Assess the morphology of the erythrocytes.
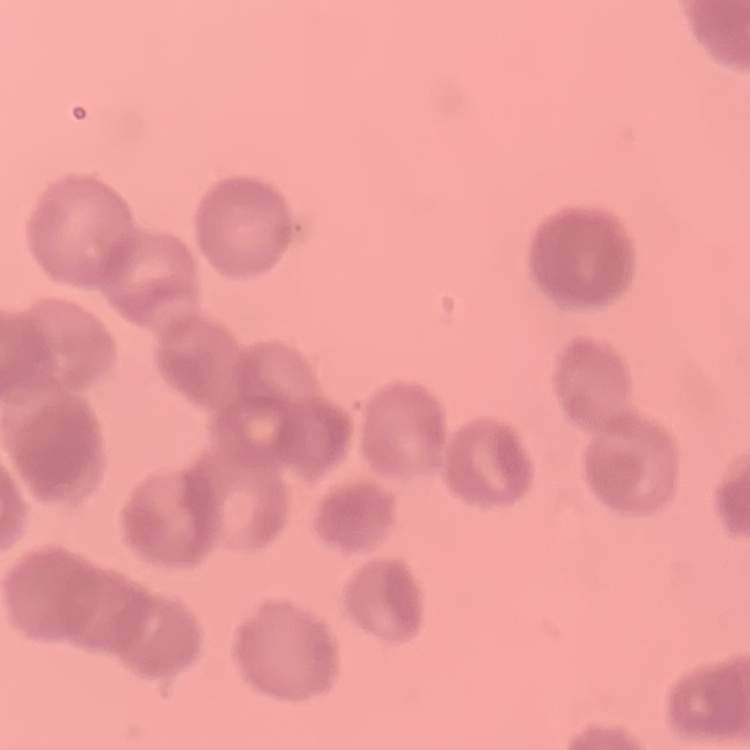
They show rouleaux formation.

Summary:
  - Preparation: thin blood smear
  - Stain: Field's or Giemsa
  - Image type: one tile cut from a larger photomicrograph